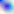 Photomicrograph. Captured at 400x magnification. Toxoplasma gondii is shown.